Outline each Plasmodium ovale-infected red blood cell.
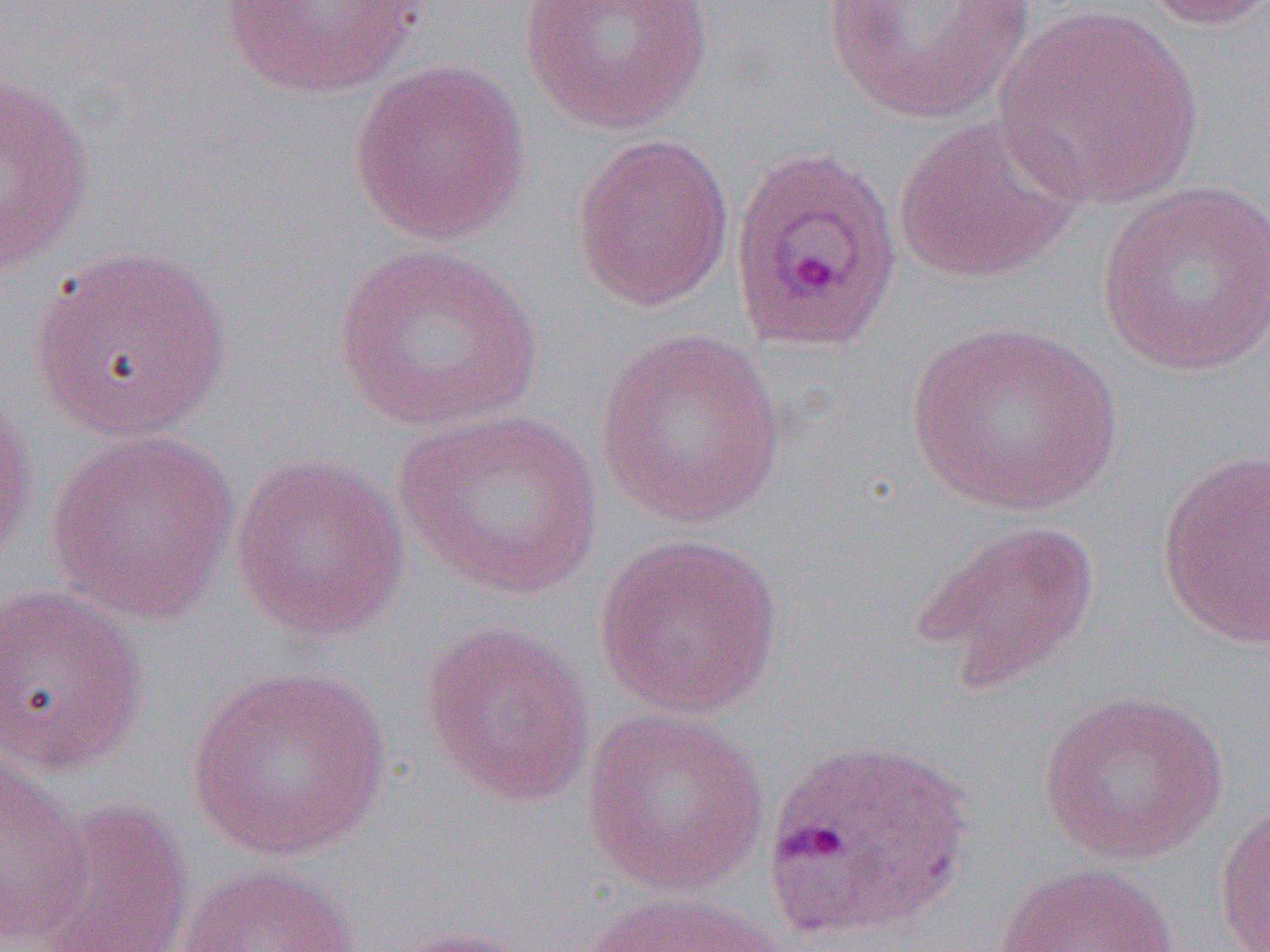

Approximate bounding boxes as named x1/y1/x2/y2 corners in pixels.
Plasmodium ovale-infected red blood cells: (x1=727, y1=147, x2=903, y2=354), (x1=762, y1=735, x2=975, y2=944).

Uninfected red blood cell locations: (x1=213, y1=0, x2=432, y2=101), (x1=518, y1=0, x2=714, y2=135), (x1=818, y1=0, x2=1037, y2=124), (x1=1133, y1=0, x2=1270, y2=31), (x1=993, y1=5, x2=1206, y2=211), (x1=347, y1=58, x2=532, y2=245), (x1=0, y1=71, x2=96, y2=274), (x1=891, y1=117, x2=1080, y2=284), (x1=570, y1=133, x2=734, y2=312), (x1=1096, y1=181, x2=1270, y2=377), (x1=333, y1=241, x2=545, y2=433), (x1=28, y1=246, x2=235, y2=443), (x1=905, y1=319, x2=1125, y2=517), (x1=592, y1=328, x2=789, y2=529), (x1=0, y1=389, x2=39, y2=568), (x1=390, y1=407, x2=607, y2=602), (x1=44, y1=430, x2=241, y2=625), (x1=1157, y1=448, x2=1269, y2=650), (x1=230, y1=453, x2=409, y2=644), (x1=911, y1=518, x2=1102, y2=689), (x1=593, y1=532, x2=785, y2=720), (x1=0, y1=582, x2=151, y2=776), (x1=420, y1=620, x2=597, y2=808), (x1=186, y1=664, x2=391, y2=863), (x1=1036, y1=689, x2=1231, y2=867), (x1=581, y1=707, x2=770, y2=898), (x1=0, y1=752, x2=91, y2=944), (x1=25, y1=797, x2=196, y2=952), (x1=1213, y1=800, x2=1270, y2=952), (x1=995, y1=861, x2=1182, y2=952), (x1=169, y1=863, x2=362, y2=952), (x1=575, y1=889, x2=792, y2=952), (x1=374, y1=925, x2=542, y2=952). Slide-level diagnosis: Plasmodium ovale. Image is 1270×952 pixels. Thin blood film. 1000x magnification. Optical microscopy. Single field of view.